Comment on the morphology of the red blood cells.
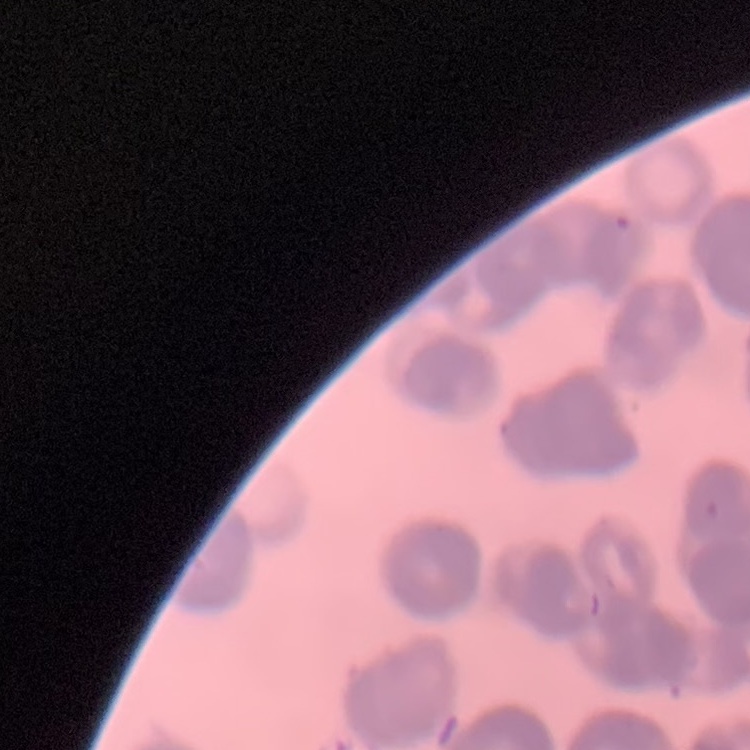

Rouleaux formation.

stain: Field's or Giemsa
image_type: square crop of a larger photomicrograph
preparation: thin blood film